Identify the blood parasite species.
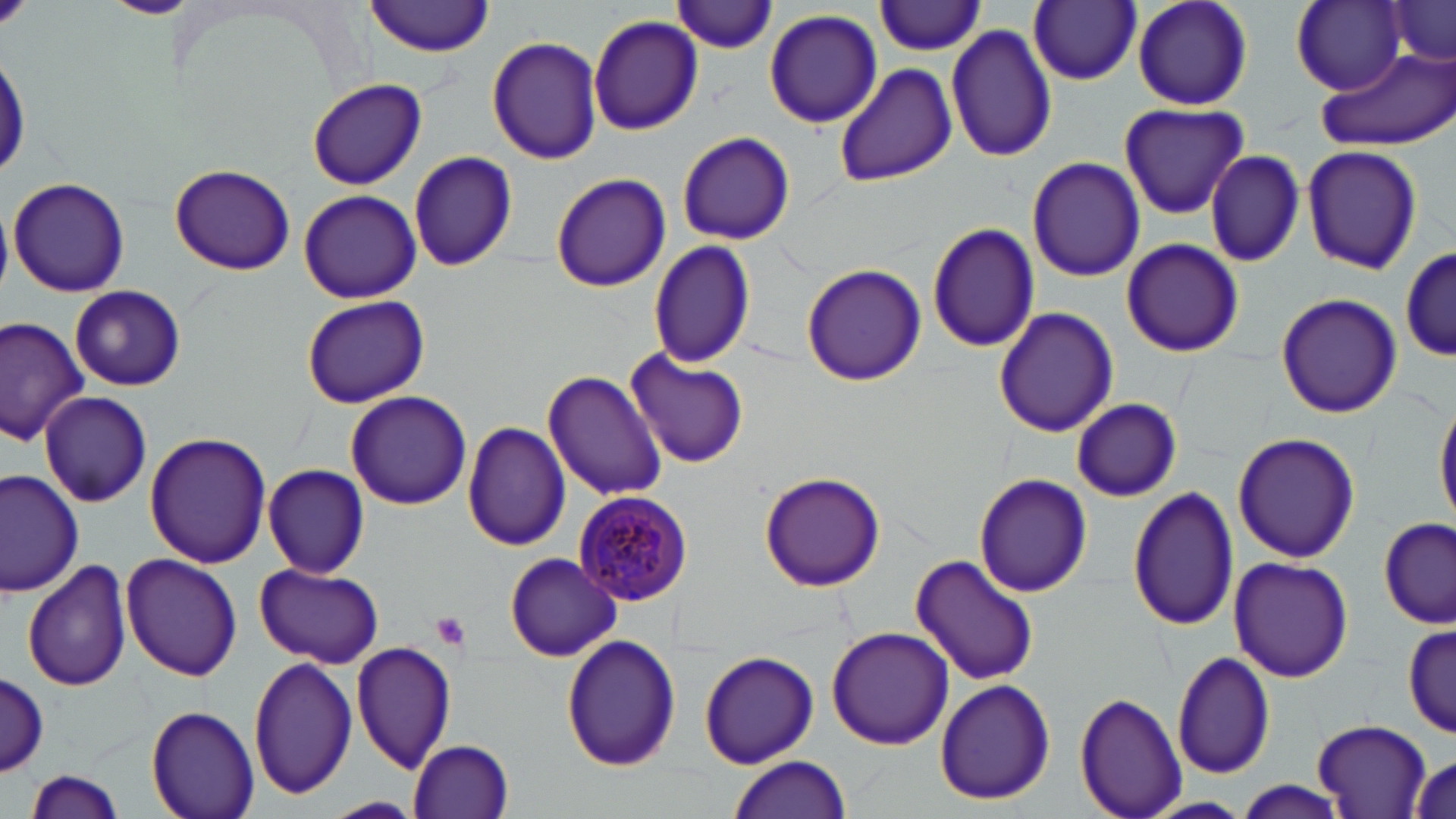

Plasmodium malariae.

Approximate bounding boxes as (x1,y1)-(x2,y2) corner pairs in pixels. Uninfected red blood cell locations: (101,0)-(197,18), (368,0)-(494,57), (675,0)-(778,54), (1131,0)-(1255,111), (1384,0)-(1456,66), (875,1)-(986,55), (1027,1)-(1140,86), (1290,2)-(1413,94), (763,8)-(882,130), (588,13)-(704,137), (946,23)-(1058,163), (487,36)-(603,166), (1318,47)-(1455,151), (833,62)-(957,188), (307,77)-(427,189), (1118,101)-(1249,219), (676,132)-(795,246), (1300,144)-(1423,275), (408,150)-(519,272), (1206,150)-(1304,267), (1026,156)-(1144,283), (169,165)-(295,275), (550,171)-(671,293), (8,178)-(129,296), (298,189)-(421,304), (0,206)-(13,297), (927,221)-(1040,354), (1120,238)-(1244,357), (648,240)-(756,370), (1399,248)-(1455,362), (801,263)-(926,387), (70,286)-(184,390), (1275,292)-(1402,420), (301,294)-(430,408), (993,307)-(1119,438), (0,316)-(92,446), (626,346)-(750,471), (543,368)-(667,504), (344,391)-(473,510), (39,392)-(152,508), (1433,394)-(1456,528), (1072,398)-(1180,502), (462,422)-(571,553), (1233,431)-(1360,563), (144,432)-(269,569), (263,463)-(370,578), (0,468)-(84,597), (760,471)-(886,593), (973,472)-(1092,597), (1128,487)-(1240,633), (1378,515)-(1453,629), (504,552)-(621,662), (910,553)-(1040,688), (121,554)-(243,680), (1228,556)-(1352,683), (21,559)-(133,693), (255,563)-(385,669), (1402,619)-(1452,738), (826,626)-(954,750), (562,636)-(681,771), (351,638)-(454,776), (698,650)-(818,768), (1172,650)-(1276,779), (247,656)-(358,802), (1,672)-(49,776), (934,678)-(1055,806), (1076,691)-(1187,818), (147,704)-(260,819), (1313,719)-(1434,816), (409,739)-(515,818), (1407,750)-(1456,817), (727,755)-(852,819), (23,770)-(129,816), (1231,781)-(1351,819), (1141,796)-(1255,818), (320,798)-(425,817). Platelet locations: (431,611)-(471,649). Plasmodium malariae-infected red blood cell locations: (573,489)-(693,605). May-Grünwald-Giemsa stain. Light microscopy. Captured at 1000x magnification. Image is 1456×819 pixels. One field of a larger specimen. Thin blood smear.